Describe the morphology of the red blood cells.
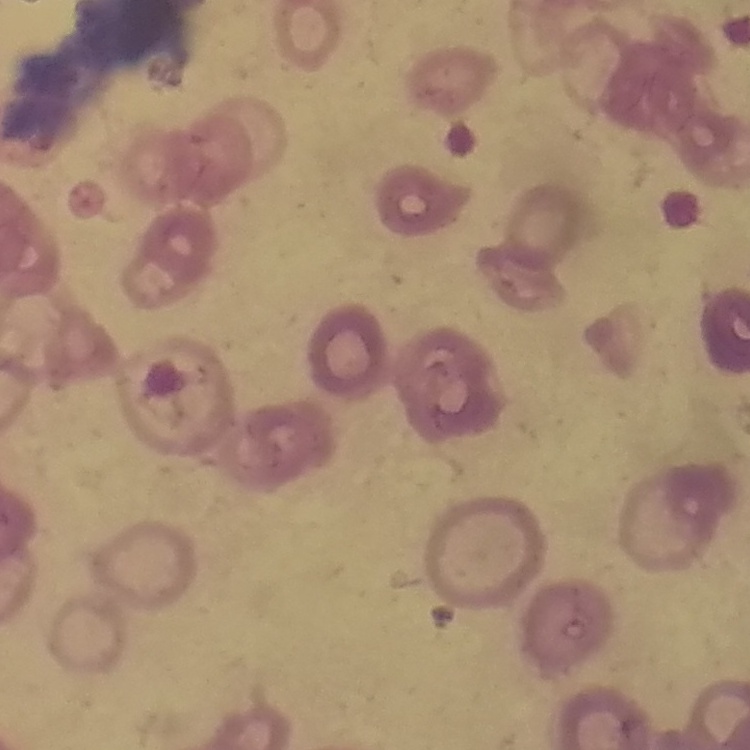

Rouleaux formation.

image type = square crop of a larger photomicrograph
stain = Field's or Giemsa
preparation = thin blood film